Describe the morphology of the erythrocytes.
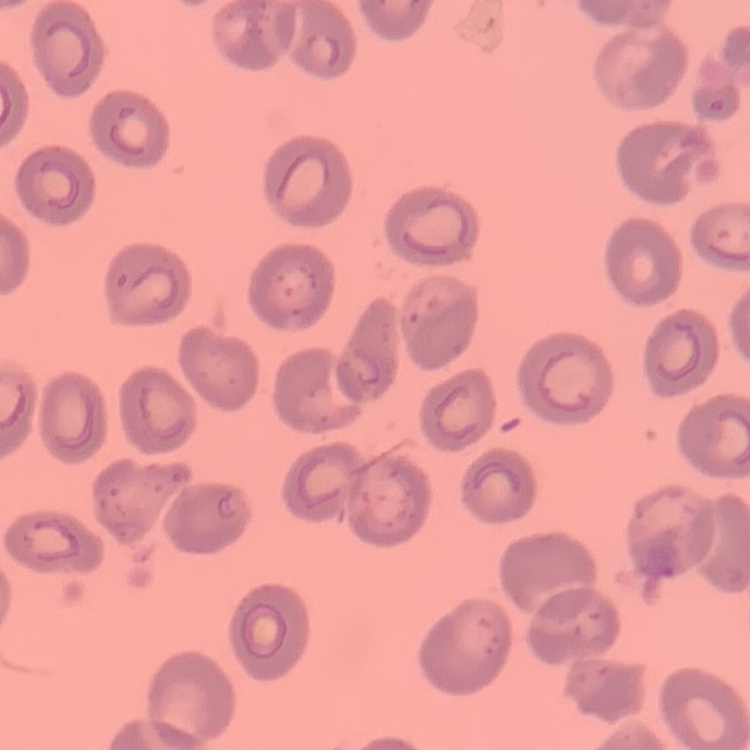
They show no rouleaux formation.

Square crop of a larger photomicrograph. Stained with either Field's or Giemsa. Thin blood film.